Report the malaria status of this cell.
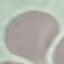

It is uninfected.

stain = Giemsa
capture = smartphone camera at the microscope eyepiece
preparation = thin blood film
image type = cell patch, automatically extracted from a larger field of view and resized to 64 × 64 pixels